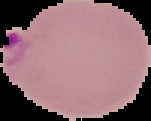
result = malaria parasites identified
image type = cell region segmented out of the field of view; surrounding area masked to black
preparation = thin blood film
image size = 151×121 pixels